State which cell type is depicted.
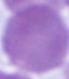
This is an erythrocyte.

modality = photomicrograph
magnification = 1000x